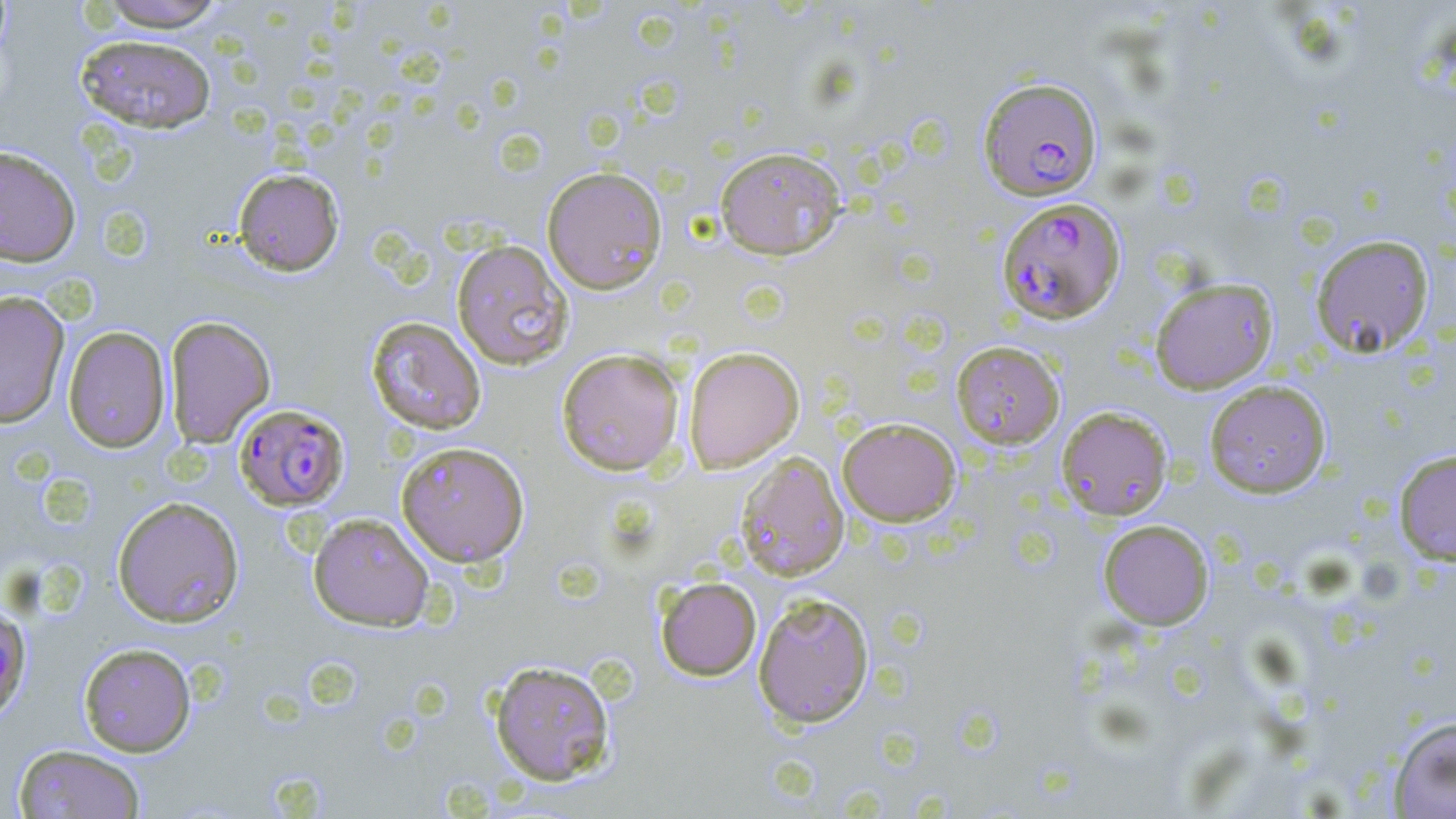 Approximate bounding boxes as (x1, y1, x2, y2) in pixels. Uninfected red blood cell locations: (96, 0, 229, 31), (75, 34, 217, 133), (0, 145, 81, 267), (714, 146, 846, 260), (542, 166, 668, 294), (233, 168, 344, 276), (1310, 234, 1434, 358), (451, 239, 574, 371), (1149, 277, 1278, 394), (0, 290, 70, 428), (164, 315, 276, 448), (365, 316, 487, 435), (62, 325, 170, 452), (951, 340, 1065, 449), (683, 346, 804, 473), (556, 348, 685, 476), (1204, 379, 1332, 498), (1056, 406, 1173, 520), (837, 417, 961, 526), (396, 441, 530, 567), (1393, 449, 1456, 565), (735, 451, 849, 581), (112, 496, 244, 627), (308, 512, 435, 631), (1098, 519, 1214, 629), (655, 576, 762, 680), (753, 592, 875, 729), (79, 642, 197, 757), (489, 660, 616, 785), (1388, 715, 1456, 818), (13, 744, 146, 818). Plasmodium falciparum-infected red blood cell locations: (978, 77, 1102, 201), (997, 196, 1126, 324), (234, 403, 350, 511), (0, 605, 33, 723). Slide-level diagnosis: Plasmodium falciparum. Thin blood film. May-Grünwald-Giemsa-stained preparation. Image is 1456×819 pixels. Single field of view. Light microscopy. 1000x magnification.